State which parasite is depicted.
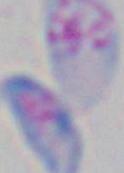

This is Toxoplasma gondii.

{
  "magnification": "1000x",
  "modality": "photomicrograph"
}